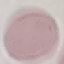

{
  "malaria_status": "uninfected",
  "image_type": "cell patch, automatically extracted from a larger field of view and resized to 64 × 64 pixels",
  "stain": "Giemsa",
  "preparation": "thin blood film",
  "capture": "smartphone camera at the microscope eyepiece"
}